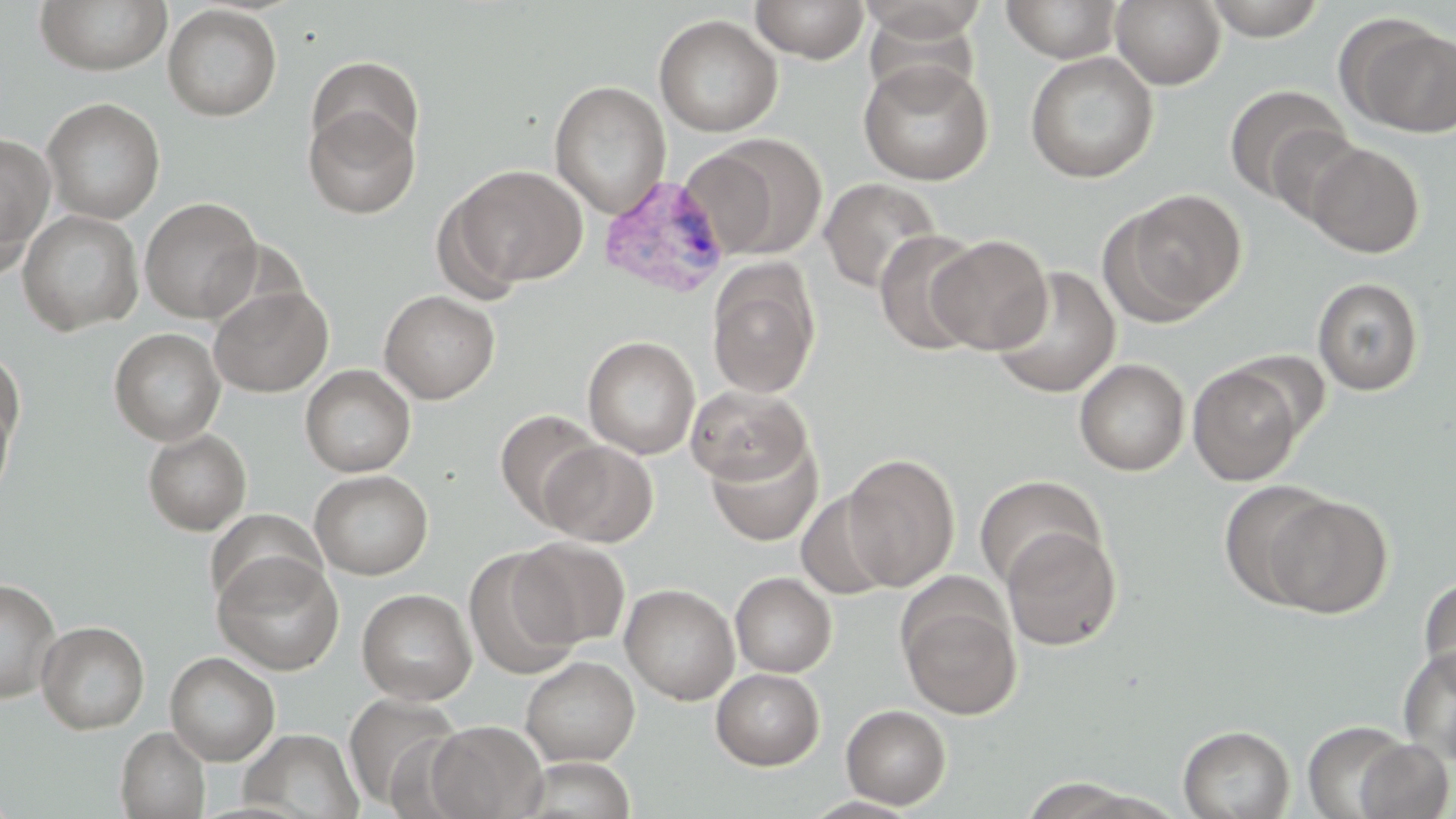

{
  "slide_level_diagnosis": "Plasmodium vivax",
  "modality": "light microscopy",
  "plasmodium_vivax_infected_red_blood_cell_locations": "approximate bounding boxes as (x1, y1, x2, y2) in pixels: (598, 174, 733, 299)",
  "preparation": "thin blood film",
  "stain": "May-Grünwald-Giemsa",
  "magnification": "1000x",
  "uninfected_red_blood_cell_locations": "approximate bounding boxes as (x1, y1, x2, y2) in pixels: (35, 0, 172, 76), (750, 0, 871, 64), (856, 0, 987, 44), (1111, 0, 1226, 89), (1201, 0, 1329, 41), (1000, 1, 1125, 63), (162, 4, 282, 121), (862, 7, 982, 105), (653, 14, 782, 136), (1344, 19, 1456, 137), (1024, 51, 1159, 183), (306, 56, 424, 169), (857, 58, 994, 185), (550, 81, 671, 217), (1224, 84, 1350, 204), (41, 97, 165, 224), (303, 101, 420, 219), (1263, 123, 1366, 227), (692, 133, 828, 261), (0, 134, 56, 257), (1305, 142, 1425, 258), (445, 165, 588, 291), (818, 177, 942, 295), (0, 187, 29, 283), (1107, 188, 1248, 322), (139, 197, 263, 323), (17, 210, 144, 336), (874, 229, 985, 355), (927, 234, 1052, 354), (706, 261, 821, 400), (990, 267, 1121, 398), (1313, 276, 1424, 395), (208, 284, 333, 397), (379, 290, 500, 404), (109, 328, 226, 445), (583, 336, 700, 460), (0, 349, 25, 452), (1075, 358, 1190, 476), (1188, 362, 1305, 486), (300, 365, 416, 477), (686, 385, 811, 485), (0, 398, 16, 506), (494, 409, 605, 526), (143, 429, 252, 536), (705, 438, 823, 546), (539, 440, 659, 547), (841, 453, 960, 590), (309, 470, 433, 580), (974, 475, 1104, 590), (1218, 481, 1337, 607), (795, 490, 899, 601), (1263, 495, 1393, 619), (206, 508, 325, 611), (1002, 526, 1122, 651), (513, 538, 630, 649), (464, 550, 581, 680), (212, 551, 345, 676), (730, 572, 837, 677), (1418, 576, 1456, 689), (0, 578, 61, 704), (620, 583, 740, 705), (357, 588, 477, 705), (899, 597, 1021, 720), (36, 620, 149, 734), (1398, 645, 1456, 764), (165, 651, 280, 765), (520, 656, 640, 766), (711, 667, 824, 770), (343, 691, 465, 810), (841, 704, 951, 809), (1303, 719, 1412, 818), (424, 720, 547, 818), (1178, 724, 1295, 819), (115, 727, 211, 818), (239, 728, 363, 818), (1354, 739, 1454, 818), (519, 757, 637, 818), (1021, 777, 1142, 818), (802, 795, 923, 818)",
  "image_size": "1456×819 pixels",
  "field_of_view": "one of a larger specimen"
}